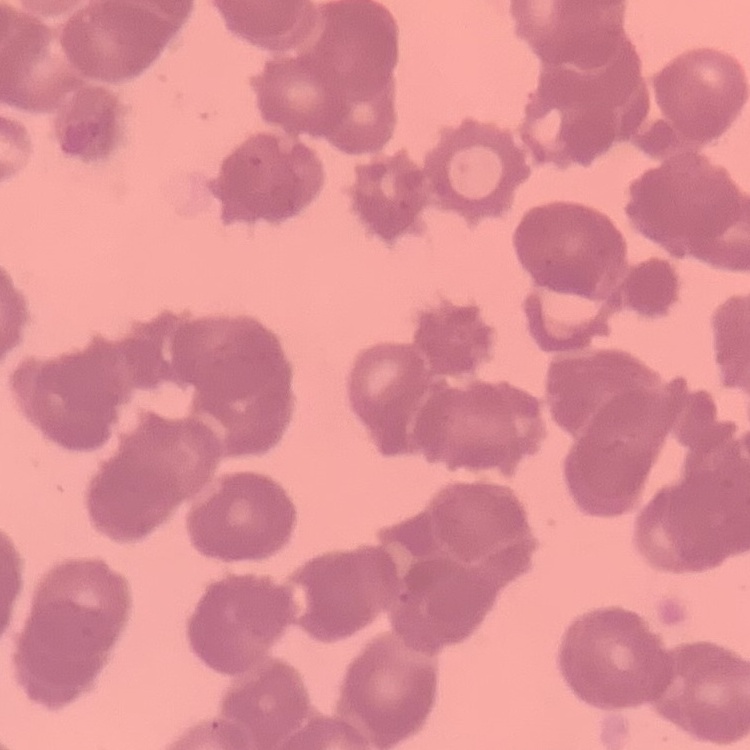

Summary:
  - Red blood cell morphology: rouleaux formation
  - Image type: square crop of a larger photomicrograph
  - Stain: Field's or Giemsa
  - Preparation: thin blood film